Locate every leukocyte (white blood cell).
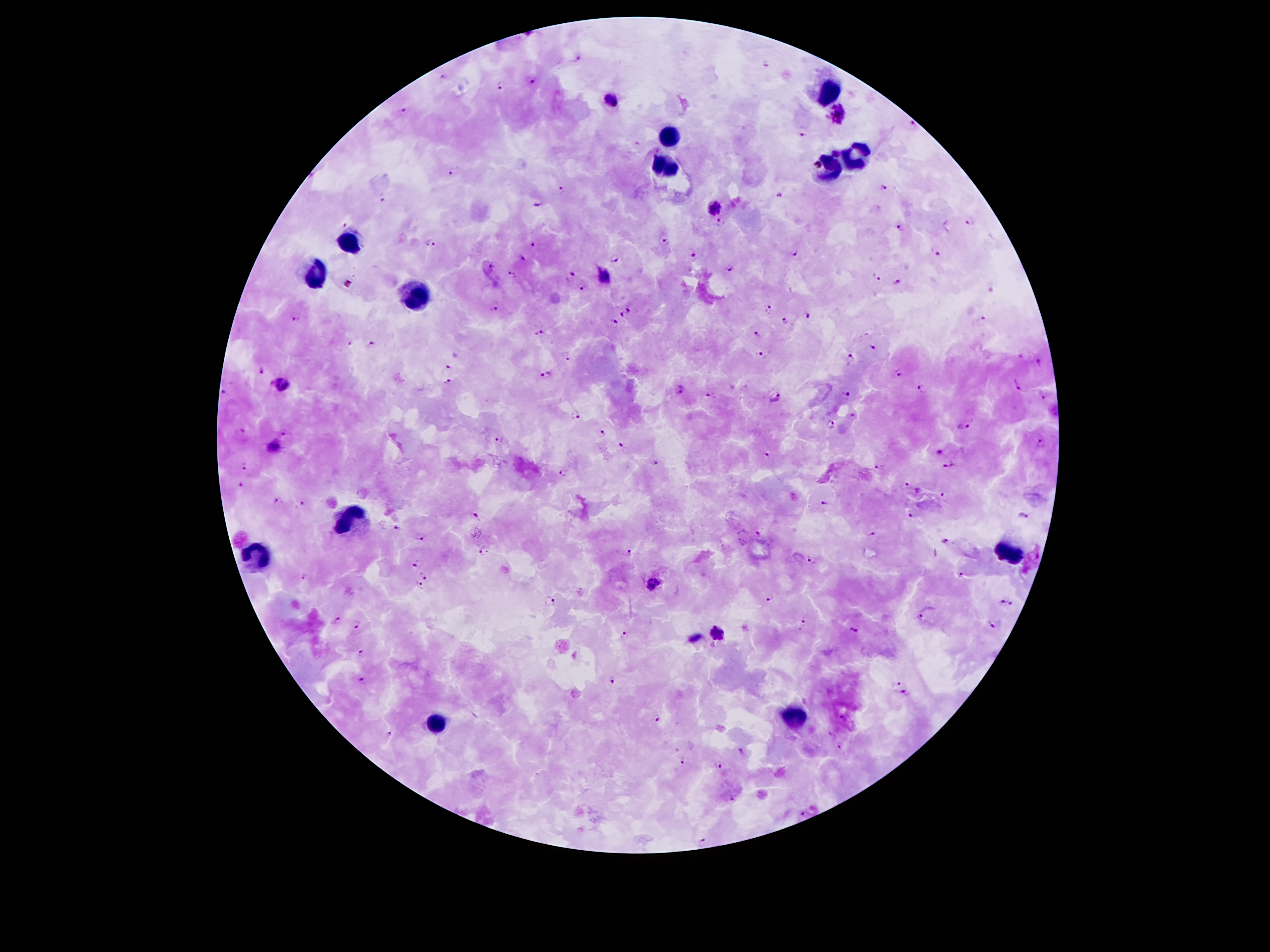

Approximate object centers, in pixels from the top-left corner.
Leukocytes: (x=830, y=94), (x=668, y=136), (x=854, y=157), (x=665, y=170), (x=828, y=171), (x=350, y=241), (x=316, y=273), (x=418, y=296), (x=353, y=517), (x=1009, y=550), (x=255, y=553), (x=794, y=716), (x=437, y=721).

Plasmodium parasite locations = (x=578, y=57), (x=766, y=63), (x=443, y=76), (x=532, y=82), (x=500, y=85), (x=612, y=101), (x=402, y=109), (x=839, y=114), (x=914, y=123), (x=804, y=130), (x=836, y=153), (x=454, y=174), (x=882, y=188), (x=561, y=191), (x=777, y=196), (x=384, y=199), (x=538, y=203), (x=715, y=206), (x=722, y=222), (x=971, y=222), (x=344, y=224), (x=899, y=226), (x=663, y=242), (x=432, y=243), (x=536, y=245), (x=934, y=252), (x=795, y=254), (x=689, y=255), (x=523, y=258), (x=613, y=259), (x=490, y=266), (x=728, y=268), (x=570, y=273), (x=514, y=274), (x=605, y=276), (x=876, y=278), (x=898, y=281), (x=583, y=287), (x=767, y=307), (x=496, y=308), (x=629, y=310), (x=622, y=314), (x=806, y=316), (x=298, y=319), (x=982, y=319), (x=782, y=321), (x=613, y=323), (x=540, y=332), (x=757, y=333), (x=371, y=344), (x=349, y=345), (x=873, y=349), (x=762, y=355), (x=565, y=357), (x=852, y=358), (x=1037, y=363), (x=448, y=366), (x=259, y=370), (x=900, y=372), (x=546, y=376), (x=446, y=380), (x=283, y=383), (x=1017, y=384), (x=922, y=388), (x=677, y=390), (x=224, y=393), (x=709, y=394), (x=846, y=395), (x=776, y=397), (x=1041, y=397), (x=576, y=416), (x=852, y=417), (x=828, y=424), (x=965, y=426), (x=241, y=431), (x=282, y=432), (x=602, y=433), (x=500, y=441), (x=1040, y=443), (x=622, y=445), (x=274, y=446), (x=938, y=452), (x=766, y=455), (x=655, y=463), (x=880, y=463), (x=244, y=465), (x=948, y=467), (x=565, y=470), (x=905, y=484), (x=240, y=485), (x=919, y=490), (x=944, y=495), (x=277, y=501), (x=827, y=501), (x=302, y=504), (x=913, y=512), (x=475, y=515), (x=1022, y=515), (x=397, y=529), (x=758, y=533), (x=874, y=534), (x=422, y=537), (x=948, y=543), (x=481, y=550), (x=629, y=551), (x=811, y=560), (x=417, y=562), (x=303, y=574), (x=424, y=574), (x=961, y=574), (x=653, y=583), (x=419, y=586), (x=769, y=597), (x=1002, y=600), (x=552, y=602), (x=1010, y=602), (x=335, y=619), (x=919, y=620), (x=357, y=625), (x=803, y=625), (x=994, y=625), (x=853, y=629), (x=625, y=633), (x=718, y=633), (x=359, y=649), (x=361, y=678), (x=613, y=678), (x=897, y=681), (x=907, y=693), (x=655, y=719), (x=842, y=719), (x=387, y=733), (x=839, y=745), (x=683, y=760), (x=719, y=765), (x=731, y=799), (x=801, y=811), (x=702, y=842)
image size = 1270×952 pixels
preparation = thick blood smear
magnification = 100x
patient malaria status = infected with Plasmodium falciparum
capture = smartphone camera through the microscope eyepiece
field of view = one from this slide
stain = Giemsa